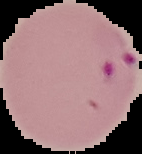
Image is 142×154 pixels. Cell region segmented out of the field of view; the surrounding area is masked to black. Malaria status: parasitized. From a thin blood smear.